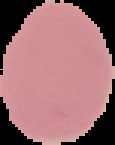

Malaria status: uninfected. Segmented cell region on a black background. From a thin blood smear. Image is 115×145 pixels.